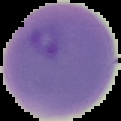 Result: Plasmodium parasites identified. Cell region segmented out of the field of view; the surrounding area is masked to black. Image is 121×121 pixels. From a thin blood smear.